Point out each malaria parasite.
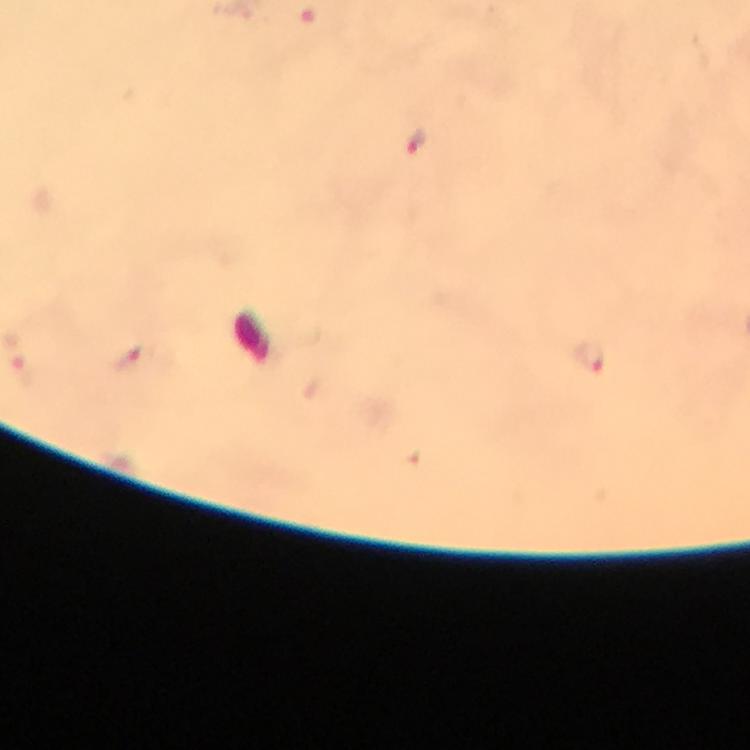

Approximate object centers, in pixels from the top-left corner.
Malaria parasites: (x=416, y=143), (x=132, y=357), (x=592, y=358).

preparation = thick blood film
magnification = 100x
context = from a malaria diagnostic workup
stain = Giemsa
image size = 750×750 pixels
immersion oil = applied
cropped from = one field of view
capture = smartphone camera through the microscope